Assess this cell for malaria.
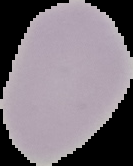
It is uninfected.

Image is 133×166 pixels. Cell region segmented out of the field of view; the surrounding area is masked to black. From a thin blood smear.